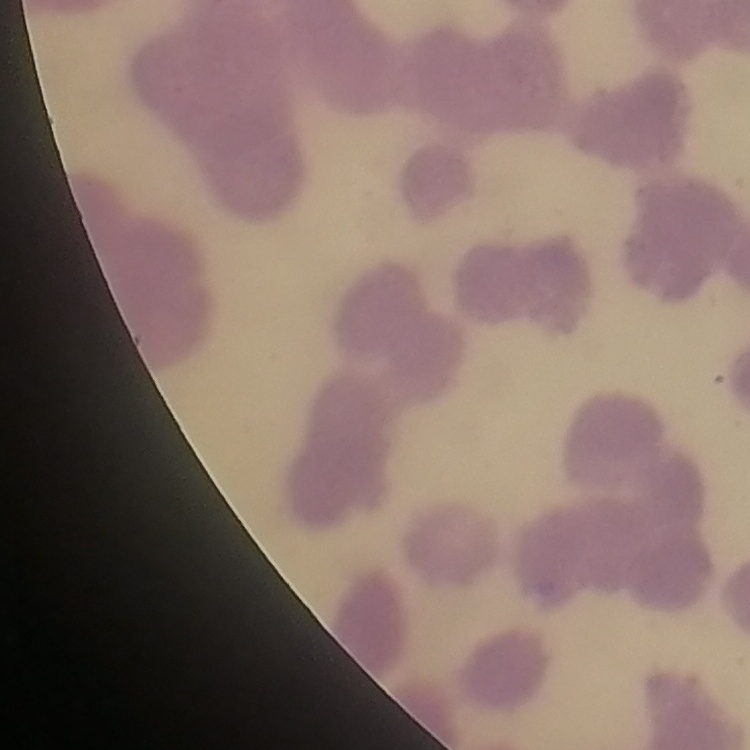

Summary:
  - Erythrocyte morphology: rouleaux formation
  - Preparation: thin blood smear
  - Image type: one tile cut from a larger photomicrograph
  - Stain: Field's or Giemsa